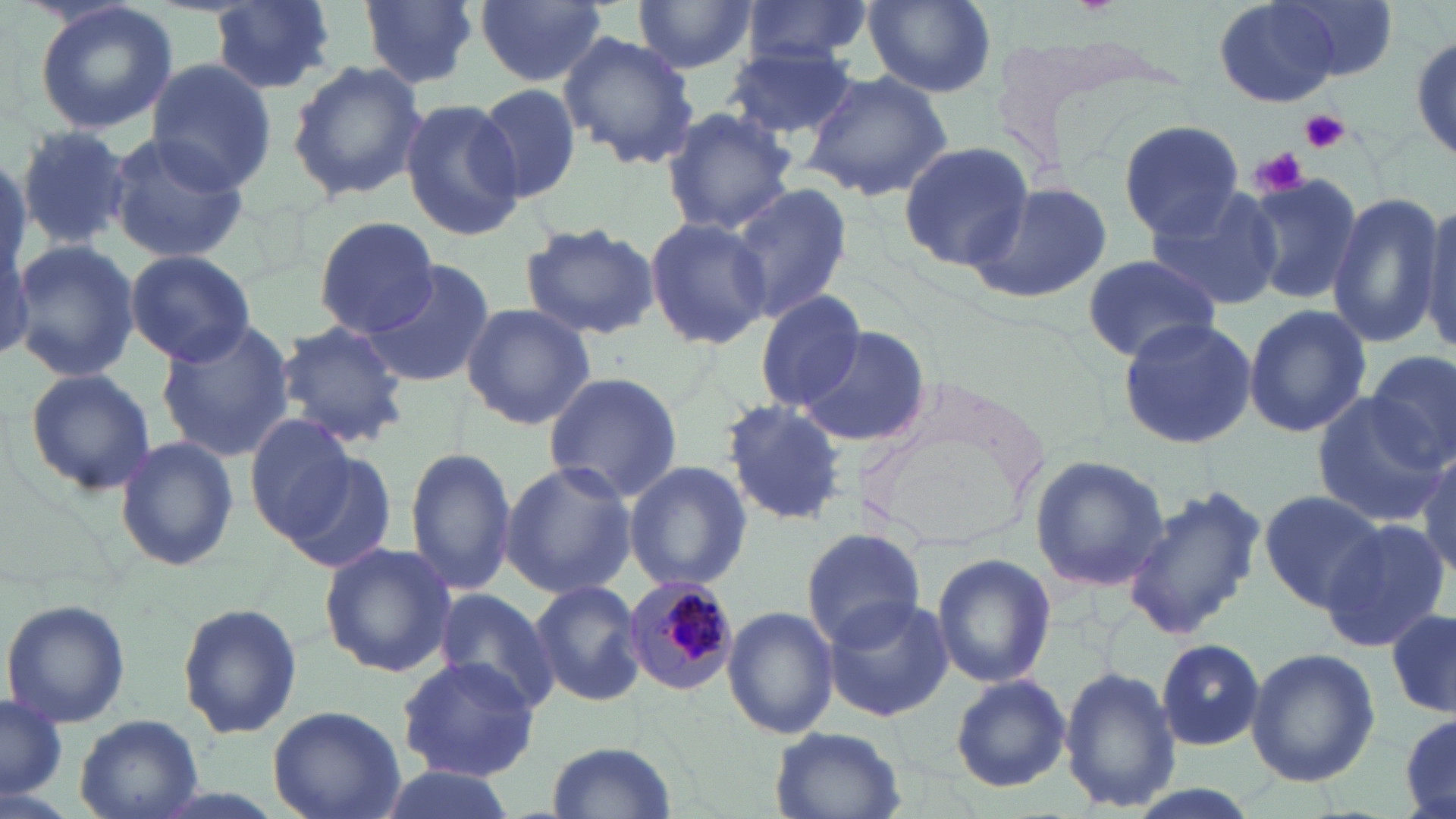
Summary:
  - Coordinate format: approximate bounding boxes as [x1, y1, x2, y2] in pixels
  - Plasmodium malariae-infected red blood cell locations: [623, 576, 740, 697]
  - Uninfected red blood cell locations: [33, 0, 178, 135], [211, 0, 338, 93], [362, 0, 480, 89], [474, 0, 610, 90], [633, 0, 758, 74], [739, 0, 872, 65], [1276, 0, 1398, 80], [1212, 1, 1348, 110], [864, 2, 994, 97], [1409, 25, 1456, 164], [557, 31, 700, 173], [727, 45, 859, 143], [288, 59, 426, 200], [146, 61, 276, 194], [800, 69, 954, 202], [472, 83, 583, 206], [400, 99, 524, 241], [660, 106, 797, 235], [1117, 115, 1247, 238], [16, 123, 133, 250], [108, 132, 248, 261], [900, 139, 1037, 273], [1243, 172, 1362, 306], [964, 178, 1113, 307], [727, 183, 855, 325], [1144, 185, 1284, 311], [1326, 193, 1445, 347], [1419, 198, 1456, 354], [644, 215, 772, 350], [314, 217, 441, 337], [517, 221, 661, 340], [0, 223, 32, 367], [11, 239, 140, 382], [124, 250, 257, 366], [1081, 252, 1222, 363], [367, 260, 494, 387], [754, 290, 867, 413], [459, 303, 596, 430], [1241, 305, 1372, 438], [1116, 315, 1257, 452], [155, 317, 296, 462], [272, 320, 409, 448], [793, 324, 930, 446], [1366, 350, 1455, 466], [22, 367, 156, 499], [542, 371, 684, 503], [850, 384, 1049, 553], [1310, 392, 1444, 526], [722, 398, 850, 527], [244, 415, 359, 541], [113, 434, 238, 573], [404, 445, 517, 598], [1415, 448, 1455, 585], [279, 451, 399, 576], [1030, 454, 1169, 592], [500, 460, 636, 599], [624, 462, 753, 592], [1119, 484, 1268, 641], [1258, 486, 1389, 612], [1320, 518, 1450, 652], [801, 527, 925, 649], [319, 541, 457, 679], [929, 553, 1057, 689], [529, 579, 648, 708], [435, 587, 558, 712], [818, 595, 955, 722], [3, 600, 131, 728], [177, 602, 303, 740], [722, 604, 837, 739], [1387, 610, 1455, 720], [1156, 637, 1265, 750], [1245, 647, 1381, 786], [396, 656, 540, 780], [1060, 665, 1180, 815], [951, 673, 1070, 792], [0, 697, 66, 797], [266, 704, 405, 819], [1398, 710, 1456, 817], [73, 714, 203, 819], [770, 728, 905, 819], [545, 740, 677, 819], [375, 767, 518, 819]
  - Platelet locations: [1299, 109, 1349, 154], [1252, 147, 1309, 197]
  - Slide-level diagnosis: Plasmodium malariae
  - Stain: May-Grünwald-Giemsa
  - Modality: optical microscopy
  - Field of view: single
  - Preparation: thin blood film
  - Magnification: 1000x
  - Image size: 1456×819 pixels